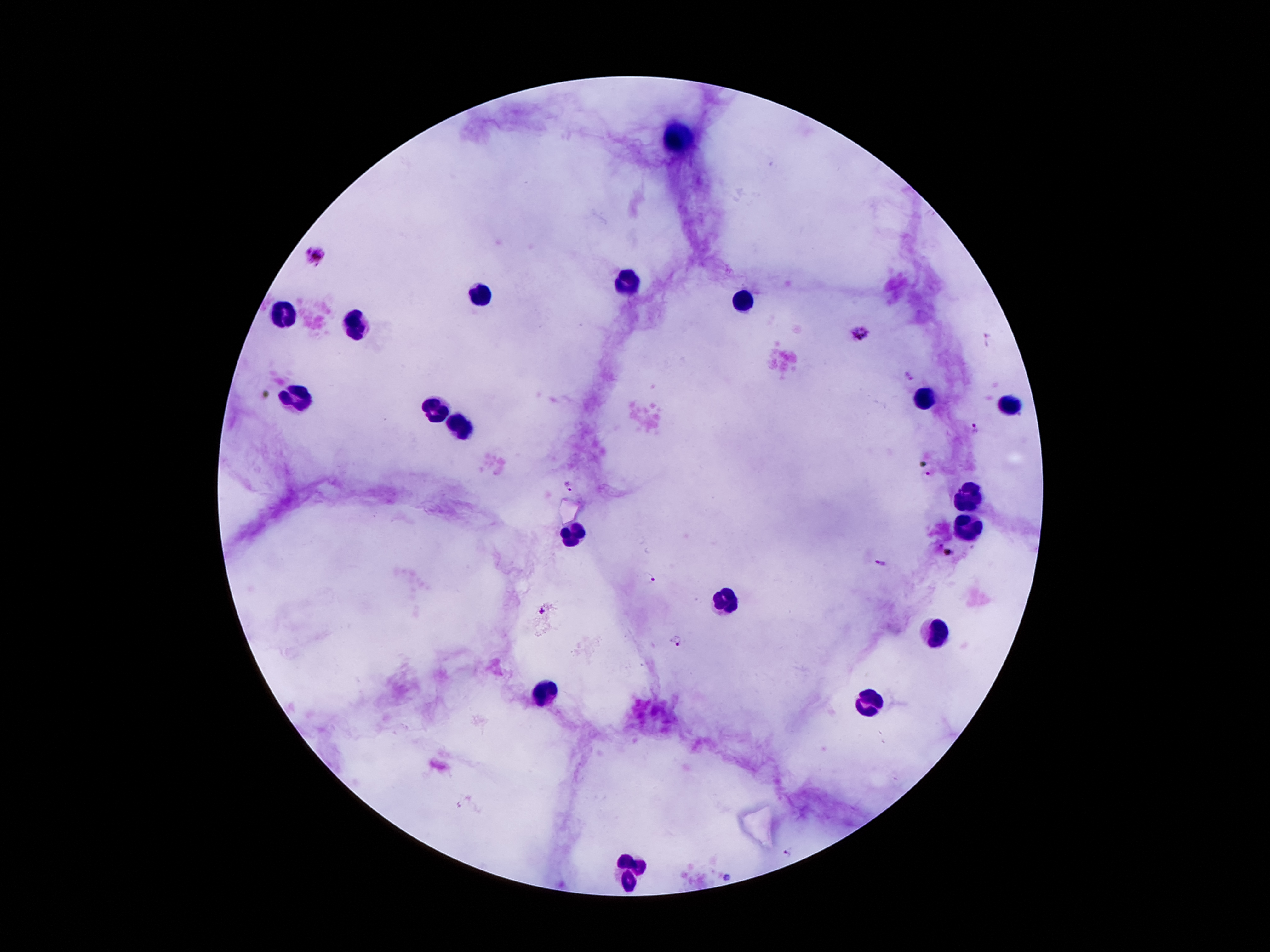
Approximate centers as [x, y] in pixels.
Summary:
  - Leukocyte locations: [680, 139], [629, 275], [487, 294], [741, 302], [283, 319], [356, 327], [928, 397], [293, 399], [434, 407], [1014, 407], [466, 428], [967, 495], [965, 529], [573, 533], [725, 597], [935, 635], [546, 695], [867, 704], [632, 870]
  - Malaria parasite locations: [315, 256], [858, 333], [909, 376], [976, 428], [929, 474], [567, 487], [948, 553], [881, 564], [651, 578], [543, 610], [678, 640], [788, 854], [726, 878]
  - Image size: 1270×952 pixels
  - Stain: Giemsa
  - Field of view: one from this slide
  - Preparation: thick blood smear
  - Capture: smartphone camera through the microscope eyepiece
  - Magnification: 100x
  - Patient malaria status: infected with Plasmodium falciparum